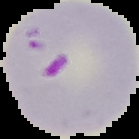

Summary:
  - Preparation: thin blood film
  - Image size: 139×139 pixels
  - Image type: segmented cell region with the area outside set to black
  - Result: malaria parasites identified